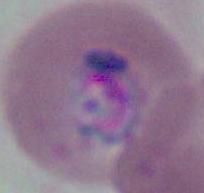
Summary:
  - Magnification: 400x or 1000x
  - Identification: Plasmodium
  - Modality: micrograph